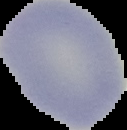
malaria status = uninfected
image size = 127×130 pixels
image type = segmented cell region on a black background
preparation = thin blood smear